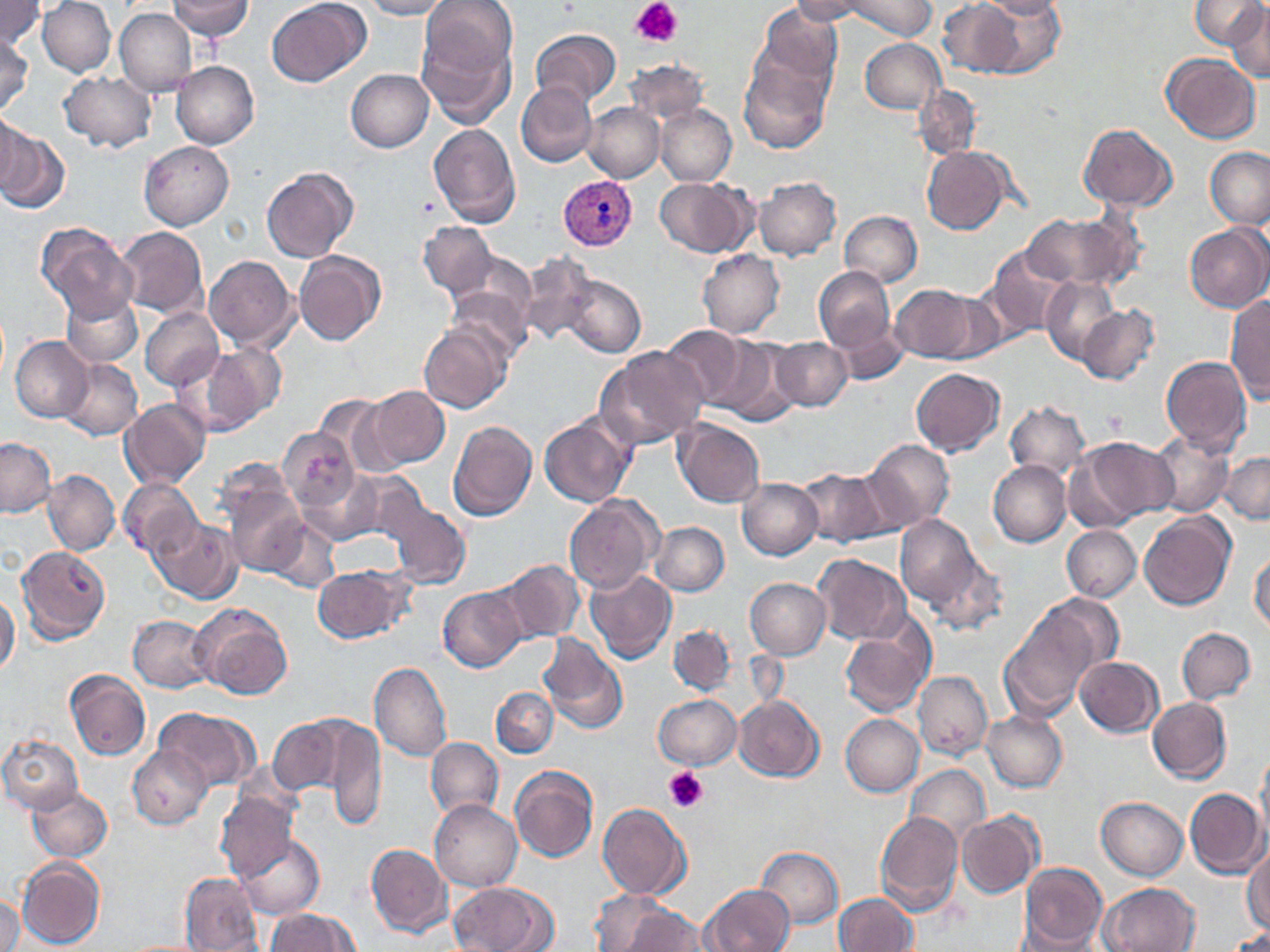
Summary:
  - Coordinate format: approximate bounding boxes as [x1, y1, x2, y2] in pixels
  - Platelet locations: [632, 0, 682, 47], [666, 767, 710, 811]
  - Plasmodium vivax-infected red blood cell locations: [558, 175, 638, 251]
  - Uninfected red blood cell locations: [0, 0, 44, 50], [37, 0, 115, 77], [167, 0, 254, 40], [359, 0, 451, 20], [421, 0, 516, 81], [789, 0, 874, 24], [847, 0, 934, 40], [939, 0, 1025, 77], [973, 0, 1066, 78], [983, 0, 1066, 20], [1190, 0, 1264, 49], [266, 1, 369, 87], [755, 2, 841, 88], [1226, 3, 1270, 82], [115, 7, 196, 96], [531, 28, 620, 108], [416, 31, 516, 128], [0, 37, 33, 113], [860, 38, 944, 114], [1162, 53, 1261, 144], [737, 55, 831, 153], [625, 59, 709, 124], [172, 61, 259, 149], [346, 69, 433, 152], [57, 71, 156, 152], [517, 81, 597, 168], [914, 85, 980, 160], [582, 102, 664, 183], [655, 105, 735, 186], [1, 109, 27, 197], [1078, 123, 1178, 209], [428, 124, 521, 227], [1, 128, 68, 214], [138, 141, 234, 230], [922, 146, 1013, 234], [1206, 147, 1270, 229], [261, 167, 357, 263], [753, 177, 841, 261], [654, 178, 751, 256], [838, 211, 923, 287], [1021, 213, 1136, 289], [418, 222, 497, 298], [1184, 222, 1270, 312], [35, 225, 135, 322], [114, 226, 207, 319], [984, 248, 1076, 338], [697, 249, 785, 338], [293, 250, 385, 345], [457, 252, 535, 329], [517, 252, 598, 347], [203, 256, 297, 350], [814, 267, 897, 354], [561, 275, 645, 358], [1040, 276, 1122, 365], [890, 284, 984, 363], [448, 287, 531, 362], [60, 291, 143, 369], [1225, 295, 1270, 405], [1076, 305, 1159, 385], [140, 307, 224, 391], [827, 313, 909, 383], [419, 321, 512, 415], [659, 325, 751, 408], [708, 335, 801, 423], [10, 336, 94, 422], [772, 338, 851, 411], [193, 343, 286, 433], [596, 346, 708, 448], [1160, 356, 1251, 456], [58, 358, 143, 440], [911, 368, 1004, 456], [365, 387, 450, 471], [314, 394, 403, 475], [120, 398, 211, 489], [1003, 402, 1089, 480], [539, 414, 636, 507], [673, 418, 764, 508], [447, 420, 536, 522], [278, 428, 359, 513], [1150, 431, 1234, 517], [1071, 436, 1175, 529], [1, 438, 55, 517], [860, 439, 954, 532], [1221, 452, 1269, 524], [214, 460, 298, 541], [988, 461, 1070, 548], [795, 467, 893, 547], [298, 468, 382, 545], [42, 469, 120, 556], [342, 470, 427, 552], [118, 478, 202, 561], [737, 478, 822, 560], [223, 482, 308, 575], [564, 495, 660, 592], [383, 497, 469, 589], [1139, 511, 1234, 610], [894, 514, 985, 611], [265, 515, 339, 593], [150, 517, 243, 604], [651, 522, 730, 596], [1061, 525, 1141, 602], [16, 546, 110, 644], [922, 550, 1008, 636], [1249, 551, 1270, 634], [814, 556, 911, 643], [497, 559, 586, 643], [313, 565, 413, 642], [584, 569, 675, 664], [744, 578, 831, 659], [438, 587, 526, 672], [0, 592, 20, 678], [1032, 593, 1123, 676], [191, 606, 291, 701], [1000, 612, 1096, 718], [129, 614, 215, 692], [840, 621, 934, 718], [668, 624, 737, 696], [1177, 627, 1255, 703], [538, 633, 627, 734], [1075, 656, 1163, 737], [368, 661, 452, 762], [65, 670, 150, 762], [914, 671, 991, 760], [490, 686, 560, 758], [652, 695, 739, 770], [733, 695, 825, 781], [1147, 697, 1231, 784], [155, 707, 259, 791], [981, 711, 1068, 792], [840, 714, 925, 796], [268, 717, 347, 796], [320, 719, 385, 832], [0, 733, 84, 816], [424, 737, 503, 819], [128, 746, 212, 829], [1255, 754, 1270, 844], [904, 765, 989, 844], [509, 766, 596, 862], [26, 786, 112, 862], [1185, 787, 1267, 878], [215, 790, 298, 883], [1096, 796, 1187, 880], [430, 800, 522, 891], [598, 804, 690, 900], [873, 811, 962, 915], [957, 813, 1042, 898], [236, 836, 326, 918], [1243, 843, 1270, 937], [366, 844, 451, 937], [757, 847, 843, 927], [17, 858, 105, 949], [1018, 863, 1108, 948], [179, 873, 263, 951], [448, 882, 553, 952], [1099, 882, 1201, 952], [701, 883, 796, 952], [590, 890, 674, 951], [1, 894, 23, 952], [834, 894, 919, 952], [621, 904, 707, 952], [267, 908, 360, 951], [1225, 929, 1270, 951]
  - Slide-level diagnosis: Plasmodium vivax
  - Stain: May-Grünwald-Giemsa
  - Image size: 1270×952 pixels
  - Modality: optical microscopy
  - Field of view: one of a larger specimen
  - Preparation: thin blood smear
  - Magnification: 1000x